Assess the morphology of the erythrocytes.
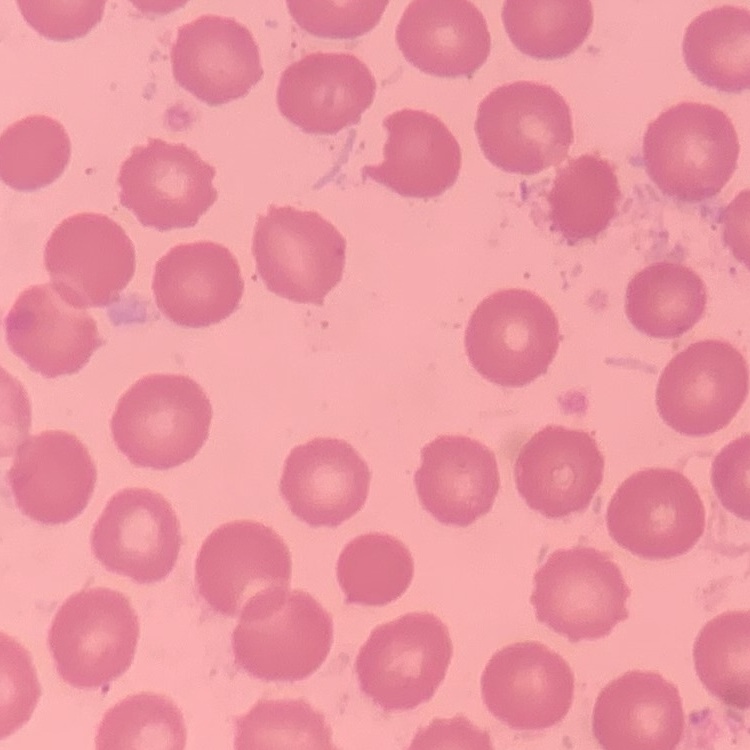
No rouleaux formation.

Summary:
  - Preparation: thin peripheral smear
  - Stain: Field's or Giemsa
  - Image type: one tile cut from a larger photomicrograph